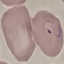

Malaria status: parasitized. Thin smear of blood. Giemsa-stained preparation. Photographed with a smartphone camera at the microscope eyepiece. Cell patch, automatically extracted from a larger field of view and resized to 64 × 64 pixels.